Describe the morphology of the red blood cells.
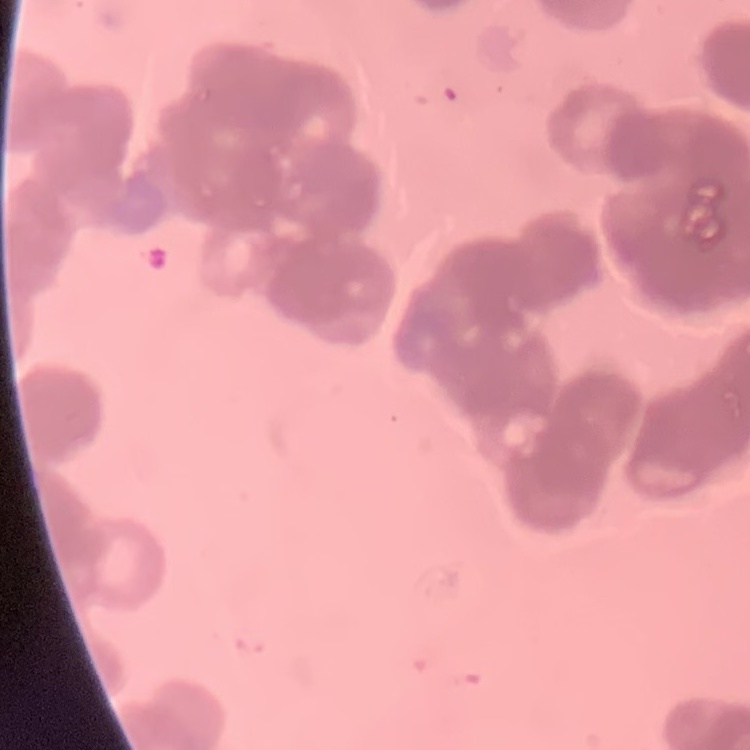
They show rouleaux formation.

Field's or Giemsa stain. One tile cut from a larger photomicrograph. Thin peripheral smear.